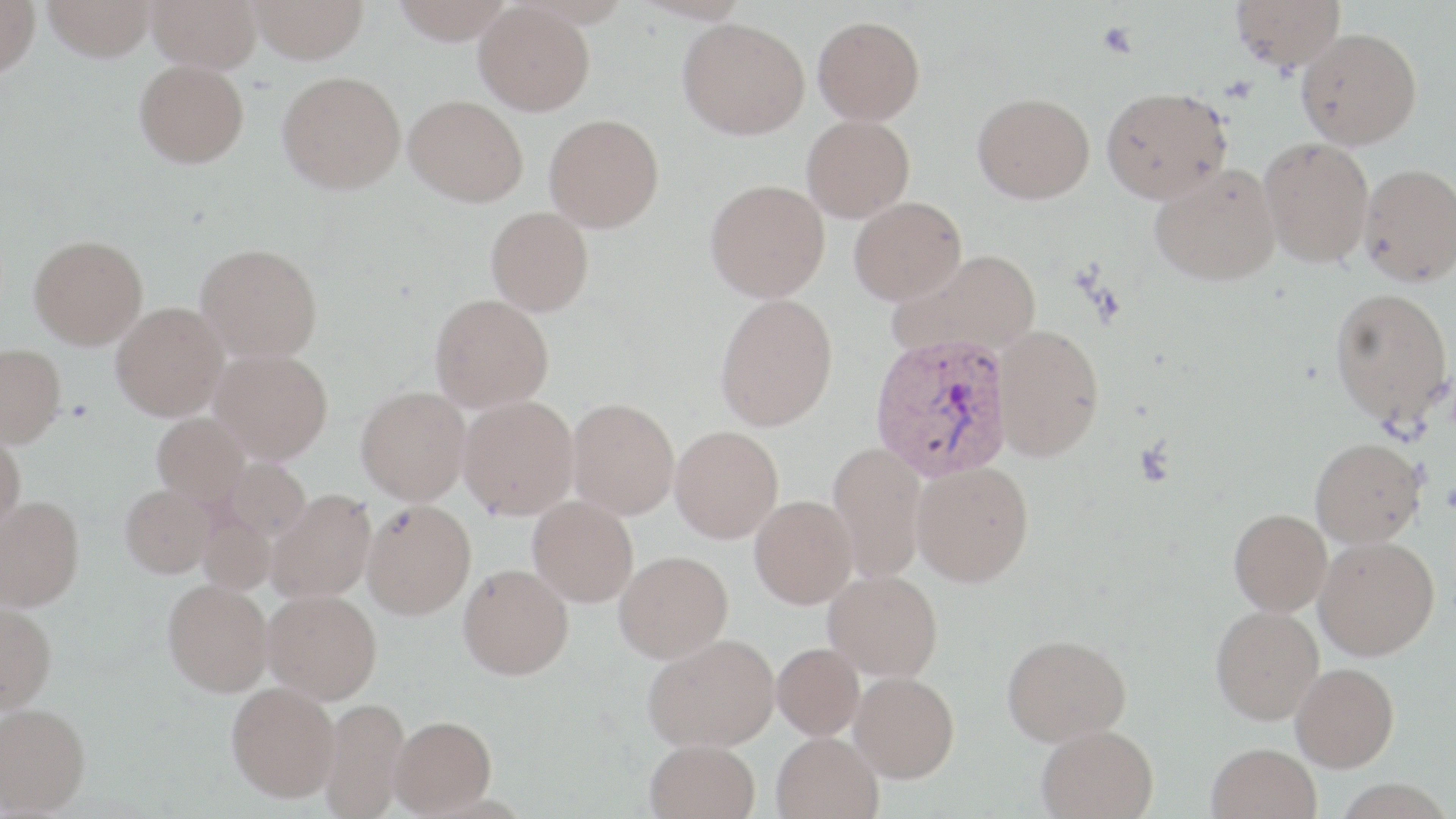

Summary:
  - Coordinate format: approximate bounding boxes as [x1, y1, x2, y2] in pixels
  - Uninfected red blood cell locations: [0, 0, 40, 76], [43, 0, 155, 61], [147, 0, 261, 72], [249, 0, 369, 63], [391, 0, 516, 44], [1231, 0, 1345, 71], [475, 2, 595, 115], [813, 15, 925, 124], [678, 18, 809, 139], [1296, 28, 1422, 148], [135, 59, 249, 167], [278, 71, 405, 193], [1101, 86, 1232, 204], [973, 92, 1095, 203], [404, 94, 528, 206], [544, 113, 664, 231], [802, 115, 915, 221], [1259, 137, 1374, 267], [1150, 163, 1281, 286], [1358, 163, 1456, 286], [705, 179, 830, 302], [848, 196, 967, 304], [485, 206, 593, 315], [29, 235, 148, 348], [196, 243, 322, 363], [892, 248, 1042, 360], [1330, 287, 1453, 428], [715, 293, 838, 432], [430, 294, 554, 412], [111, 303, 229, 422], [994, 324, 1104, 460], [0, 343, 66, 448], [209, 349, 332, 465], [356, 387, 470, 505], [458, 396, 579, 520], [567, 398, 679, 520], [152, 414, 251, 510], [670, 426, 783, 544], [0, 429, 26, 536], [1310, 437, 1425, 547], [827, 443, 927, 583], [219, 459, 310, 545], [912, 460, 1034, 587], [120, 485, 217, 579], [268, 490, 376, 604], [0, 496, 84, 611], [528, 496, 638, 607], [750, 497, 858, 610], [362, 500, 475, 620], [1229, 508, 1332, 615], [197, 511, 279, 597], [1314, 536, 1440, 660], [614, 551, 733, 665], [458, 563, 574, 681], [823, 570, 942, 681], [163, 579, 272, 696], [262, 590, 382, 705], [0, 602, 56, 714], [1211, 605, 1324, 724], [1002, 634, 1131, 745], [645, 635, 779, 754], [772, 645, 865, 742], [1291, 662, 1399, 771], [850, 671, 959, 784], [226, 681, 340, 803], [319, 698, 410, 818], [0, 703, 90, 816], [390, 716, 497, 817], [1037, 725, 1159, 819], [772, 733, 883, 819], [645, 740, 760, 819], [1207, 743, 1321, 819]
  - Plasmodium vivax-infected red blood cell locations: [868, 334, 1013, 483]
  - Platelet locations: [1097, 22, 1138, 58]
  - Slide-level diagnosis: Plasmodium vivax
  - Magnification: 1000x
  - Modality: optical microscopy
  - Field of view: single
  - Image size: 1456×819 pixels
  - Stain: May-Grünwald-Giemsa
  - Preparation: thin blood smear